Outline each Plasmodium vivax-infected red blood cell.
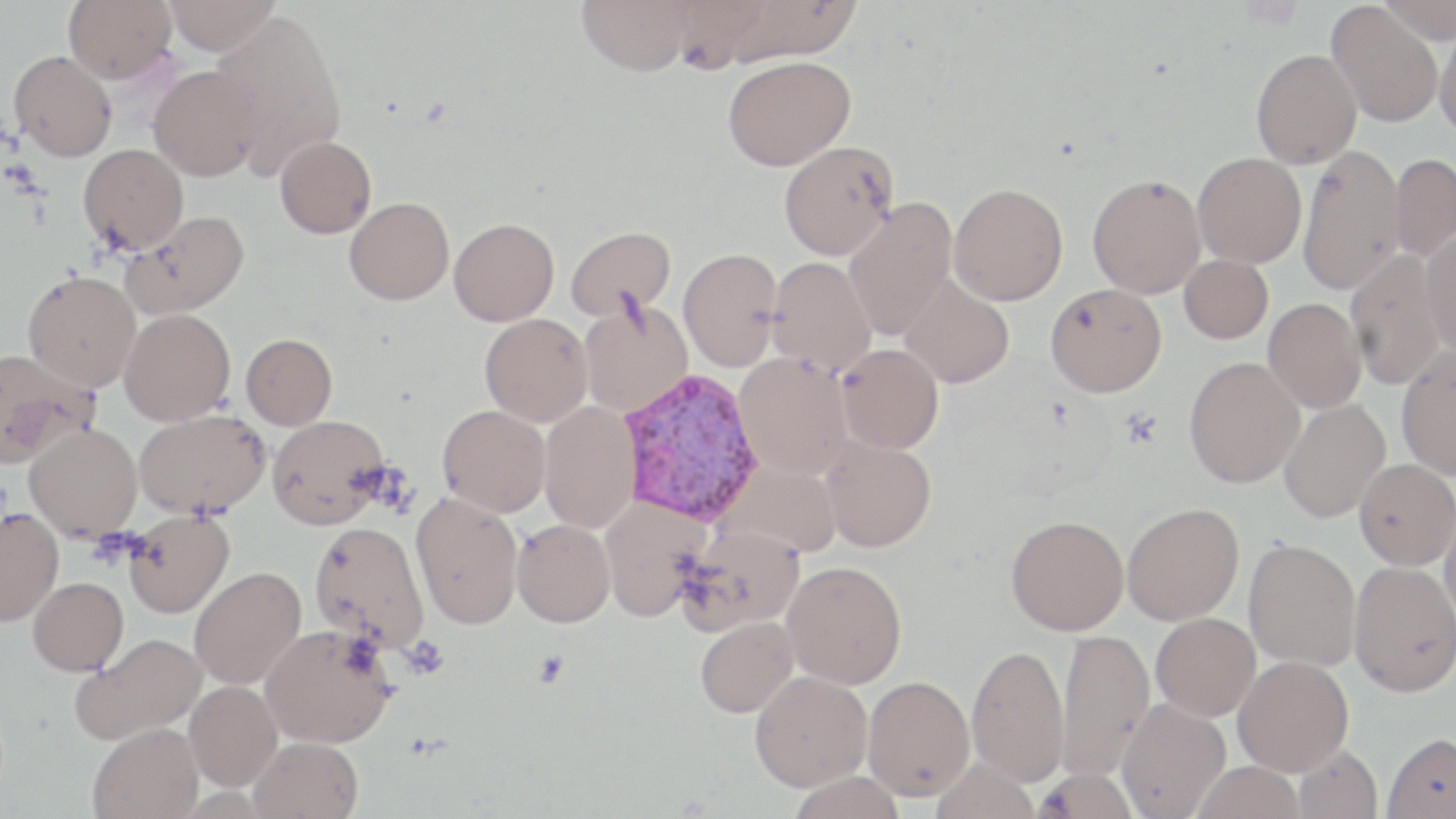
Approximate bounding boxes as (x1, y1, x2, y2) in pixels.
Plasmodium vivax-infected red blood cells: (617, 368, 764, 526).

Uninfected red blood cell locations: (63, 0, 177, 83), (164, 0, 279, 55), (577, 0, 694, 76), (663, 0, 770, 75), (719, 0, 864, 65), (1376, 0, 1456, 44), (1326, 3, 1443, 127), (211, 12, 347, 177), (1433, 21, 1456, 139), (1251, 48, 1362, 168), (9, 50, 117, 162), (723, 56, 856, 170), (148, 64, 266, 181), (275, 135, 377, 238), (778, 141, 899, 260), (78, 144, 189, 253), (1297, 144, 1405, 295), (1192, 152, 1306, 267), (1388, 153, 1456, 263), (1087, 173, 1206, 298), (948, 183, 1068, 305), (344, 197, 454, 305), (843, 198, 958, 340), (122, 210, 250, 320), (449, 217, 559, 326), (565, 226, 677, 321), (1420, 229, 1456, 357), (679, 248, 783, 371), (1345, 250, 1446, 389), (1179, 254, 1273, 344), (767, 257, 876, 375), (22, 270, 141, 391), (898, 275, 1015, 388), (1045, 283, 1167, 397), (578, 297, 694, 418), (1262, 298, 1367, 413), (119, 308, 235, 425), (480, 314, 593, 426), (241, 333, 337, 429), (837, 344, 944, 453), (1395, 346, 1456, 481), (0, 347, 98, 467), (734, 352, 853, 480), (1183, 356, 1305, 487), (1279, 398, 1390, 522), (539, 403, 640, 533), (437, 405, 551, 517), (134, 409, 269, 519), (267, 414, 389, 529), (25, 423, 142, 541), (820, 435, 937, 552), (1354, 459, 1456, 570), (720, 462, 844, 557), (411, 492, 524, 630), (599, 496, 710, 623), (1122, 502, 1244, 625), (0, 507, 63, 626), (1438, 508, 1456, 627), (125, 510, 234, 618), (1006, 514, 1129, 635), (512, 519, 615, 628), (309, 520, 430, 652), (677, 523, 805, 636), (1243, 537, 1361, 671), (782, 561, 907, 689), (1348, 561, 1456, 697), (189, 567, 306, 690), (28, 577, 129, 676), (1151, 612, 1261, 721), (695, 616, 798, 718), (260, 624, 396, 748), (1057, 628, 1155, 781), (73, 633, 207, 745), (967, 643, 1070, 787), (1233, 655, 1353, 776), (750, 670, 873, 791), (863, 675, 975, 801), (185, 681, 282, 791), (1118, 698, 1231, 819), (88, 722, 204, 819), (1381, 731, 1456, 818), (249, 736, 363, 819), (1292, 745, 1383, 819), (930, 757, 1040, 819), (1190, 761, 1306, 819), (1035, 768, 1139, 819), (786, 770, 907, 819). Platelet locations: (1120, 407, 1164, 448). Slide-level diagnosis: Plasmodium vivax. Single field of view. Light microscopy. May-Grünwald-Giemsa stain. Thin blood smear. Image is 1456×819 pixels. Captured at 1000x magnification.